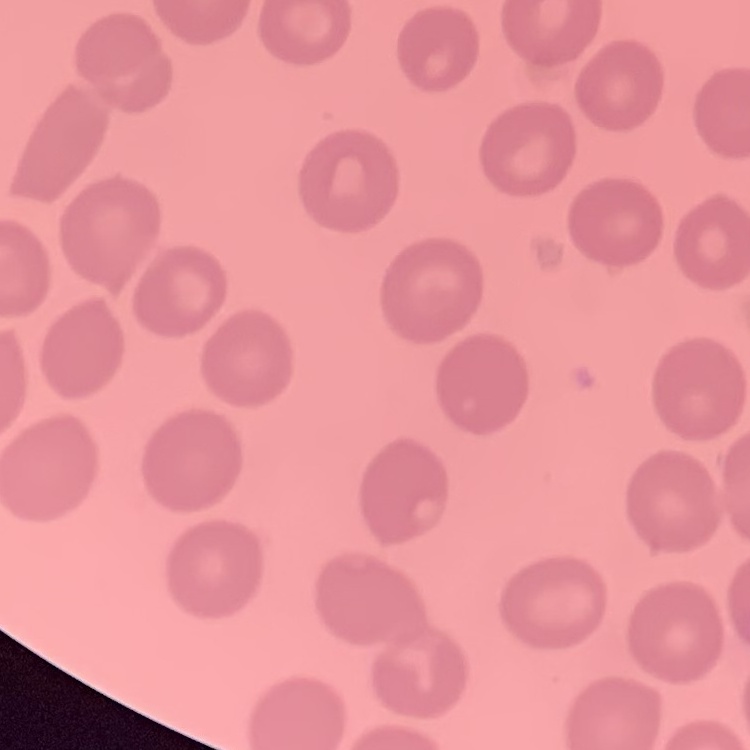
Summary:
  - Erythrocyte morphology: no rouleaux formation
  - Image type: one tile cut from a larger photomicrograph
  - Stain: Field's or Giemsa
  - Preparation: thin peripheral smear